Give the position of every Plasmodium parasite.
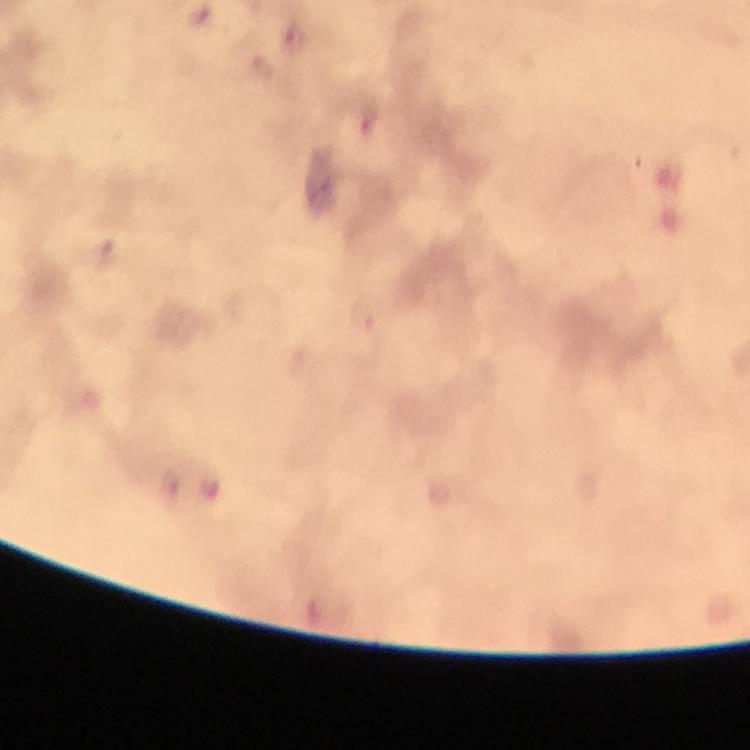

Approximate centers as {x, y} in pixels.
Plasmodium parasites: {294, 38}, {368, 121}, {210, 486}, {169, 489}.

cropped from = a single field of view
preparation = thick blood smear
image size = 750×750 pixels
magnification = 100x
capture = smartphone photograph through a microscope
immersion oil = applied
stain = Giemsa
context = from a diagnostic examination for malaria